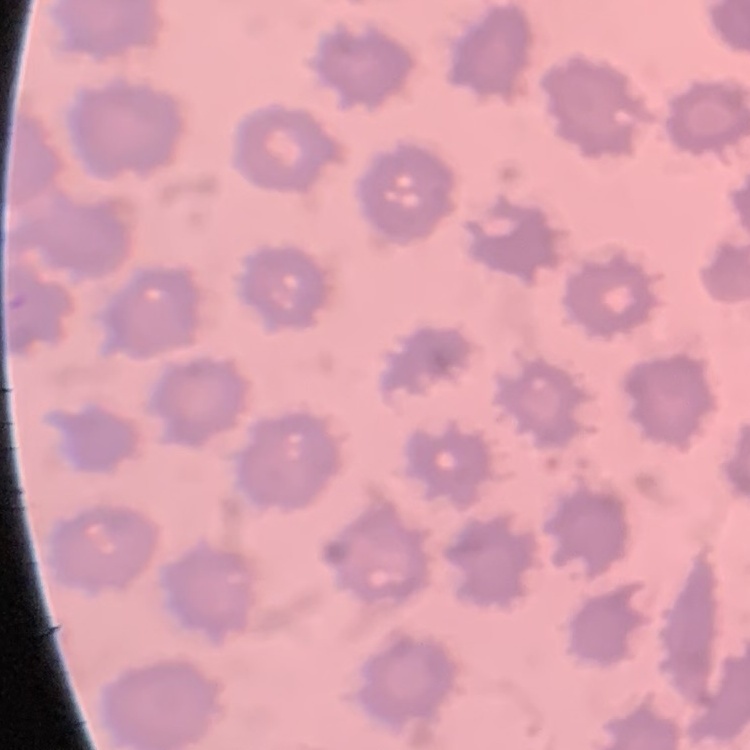
Summary:
  - Erythrocyte morphology: no rouleaux formation
  - Preparation: thin blood smear
  - Image type: one tile cut from a larger photomicrograph
  - Stain: Field's or Giemsa